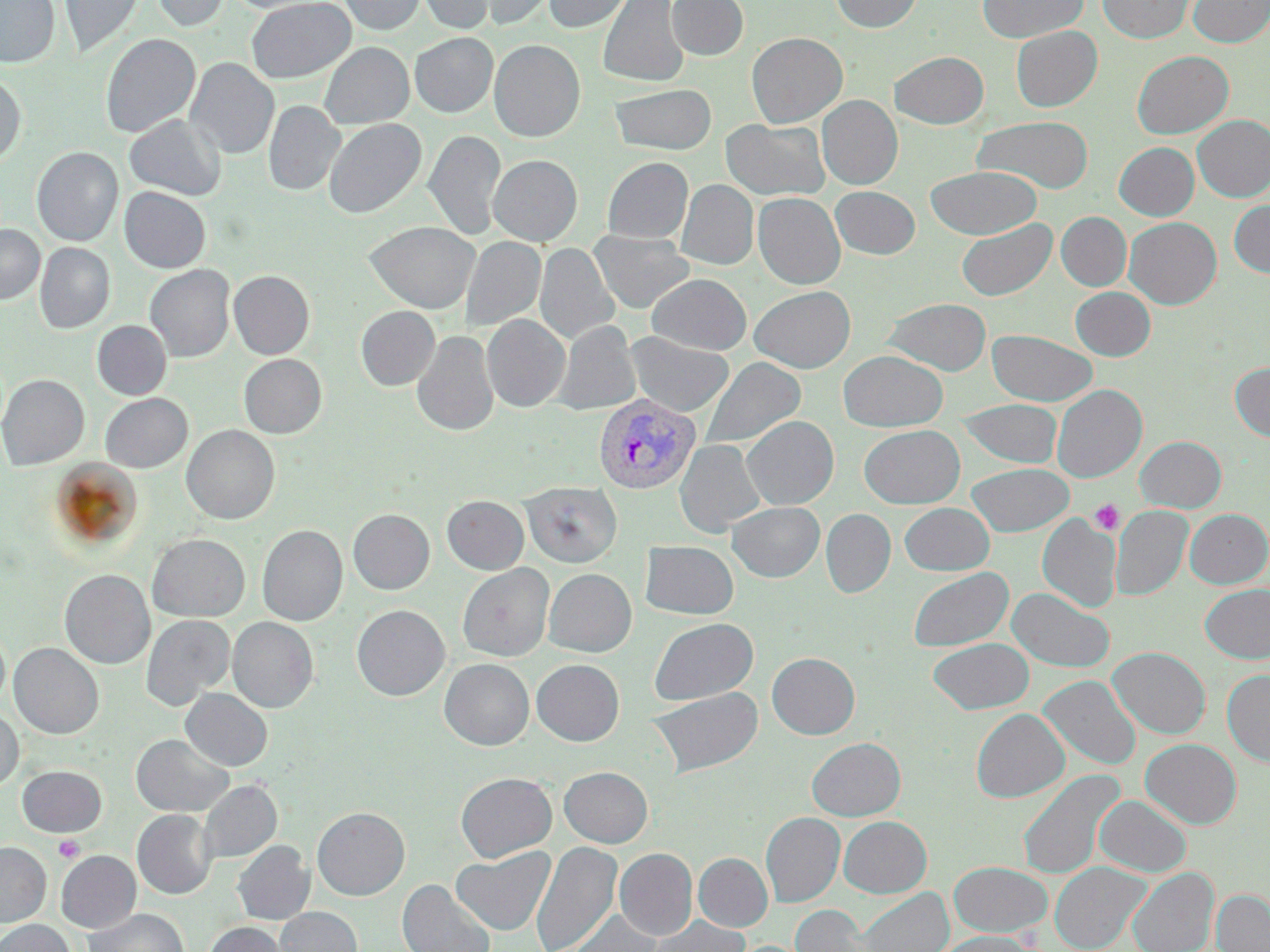
slide-level diagnosis = Plasmodium vivax
platelet locations = approximate bounding boxes as (x1, y1, x2, y2) in pixels: (1089, 500, 1124, 535), (53, 834, 85, 863)
magnification = 1000x
modality = optical microscopy
field of view = one of a larger specimen
stain = May-Grünwald-Giemsa
preparation = thin blood film
uninfected red blood cell locations = approximate bounding boxes as (x1, y1, x2, y2) in pixels: (0, 0, 59, 68), (59, 0, 144, 58), (151, 0, 230, 32), (226, 0, 330, 14), (247, 0, 355, 83), (339, 0, 426, 34), (417, 0, 497, 34), (458, 0, 556, 31), (543, 0, 634, 33), (598, 0, 688, 87), (667, 0, 748, 60), (831, 0, 923, 33), (979, 0, 1087, 42), (1097, 0, 1195, 43), (1188, 0, 1270, 47), (1011, 26, 1102, 111), (410, 32, 497, 117), (747, 32, 847, 127), (100, 33, 200, 139), (489, 40, 585, 142), (320, 42, 414, 128), (1132, 50, 1233, 139), (890, 51, 988, 129), (185, 58, 279, 159), (0, 75, 26, 165), (610, 83, 717, 154), (817, 95, 902, 189), (263, 101, 345, 196), (124, 113, 226, 200), (1193, 115, 1270, 202), (972, 116, 1093, 194), (324, 118, 426, 218), (721, 119, 829, 200), (424, 129, 506, 240), (1114, 142, 1198, 220), (32, 147, 123, 246), (488, 155, 582, 246), (602, 157, 693, 243), (926, 166, 1041, 239), (676, 180, 758, 270), (830, 186, 920, 259), (119, 187, 211, 273), (753, 192, 845, 289), (1229, 200, 1270, 278), (1056, 212, 1131, 291), (1124, 217, 1222, 309), (956, 218, 1056, 300), (365, 221, 480, 313), (0, 225, 45, 304), (590, 231, 695, 313), (460, 236, 545, 332), (35, 243, 115, 333), (535, 243, 620, 345), (145, 264, 235, 362), (229, 270, 315, 359), (647, 274, 751, 354), (749, 285, 855, 373), (1071, 287, 1155, 360), (884, 298, 991, 375), (356, 306, 440, 390), (482, 314, 570, 412), (552, 320, 640, 415), (92, 321, 171, 400), (988, 330, 1097, 406), (412, 331, 498, 436), (625, 332, 734, 417), (838, 350, 948, 431), (239, 354, 326, 438), (700, 357, 805, 450), (1230, 363, 1270, 442), (0, 374, 89, 470), (1052, 385, 1147, 482), (100, 393, 192, 473), (958, 399, 1062, 468), (742, 416, 839, 510), (182, 425, 280, 524), (859, 425, 964, 508), (1135, 436, 1226, 512), (675, 439, 766, 537), (967, 463, 1074, 536), (520, 481, 622, 567), (442, 495, 529, 574), (727, 502, 825, 582), (900, 503, 994, 575), (1112, 506, 1192, 600), (348, 509, 434, 594), (821, 509, 895, 597), (1185, 509, 1270, 588), (1037, 514, 1121, 612), (257, 525, 347, 626), (147, 534, 249, 622), (640, 541, 738, 619), (457, 563, 554, 661), (908, 567, 1013, 651), (544, 568, 636, 657), (60, 570, 155, 669), (1200, 583, 1270, 663), (1007, 588, 1114, 672), (352, 605, 450, 700), (141, 614, 234, 710), (227, 617, 318, 712), (649, 618, 758, 705), (0, 626, 10, 709), (928, 638, 1034, 714), (9, 643, 103, 739), (1108, 647, 1210, 739), (767, 652, 860, 739), (439, 658, 534, 750), (531, 659, 624, 746), (1222, 669, 1270, 766), (1039, 675, 1141, 769), (647, 686, 764, 777), (181, 688, 273, 771), (0, 708, 23, 792), (971, 708, 1069, 802), (132, 735, 234, 816), (807, 738, 906, 821), (1140, 739, 1241, 829), (18, 766, 106, 836), (559, 766, 653, 847), (1017, 770, 1123, 881), (456, 772, 556, 862), (199, 780, 281, 863), (1094, 795, 1191, 877), (312, 807, 409, 900), (132, 810, 217, 899), (761, 812, 845, 906), (838, 816, 932, 897), (232, 840, 314, 925), (530, 840, 622, 952), (0, 842, 51, 926), (451, 846, 556, 935), (614, 848, 698, 940), (56, 851, 141, 932), (694, 853, 772, 932), (949, 862, 1052, 938), (1050, 862, 1149, 952), (1128, 868, 1218, 952), (397, 879, 496, 952), (856, 888, 953, 952), (1212, 889, 1270, 952), (790, 904, 874, 952), (85, 907, 189, 952), (274, 907, 361, 952), (563, 908, 662, 952), (648, 916, 749, 952), (0, 919, 74, 952), (205, 922, 290, 952), (934, 931, 1040, 952)
Plasmodium vivax-infected red blood cell locations = approximate bounding boxes as (x1, y1, x2, y2) in pixels: (593, 393, 701, 493)
image size = 1270×952 pixels